Outline each Plasmodium vivax-infected red blood cell.
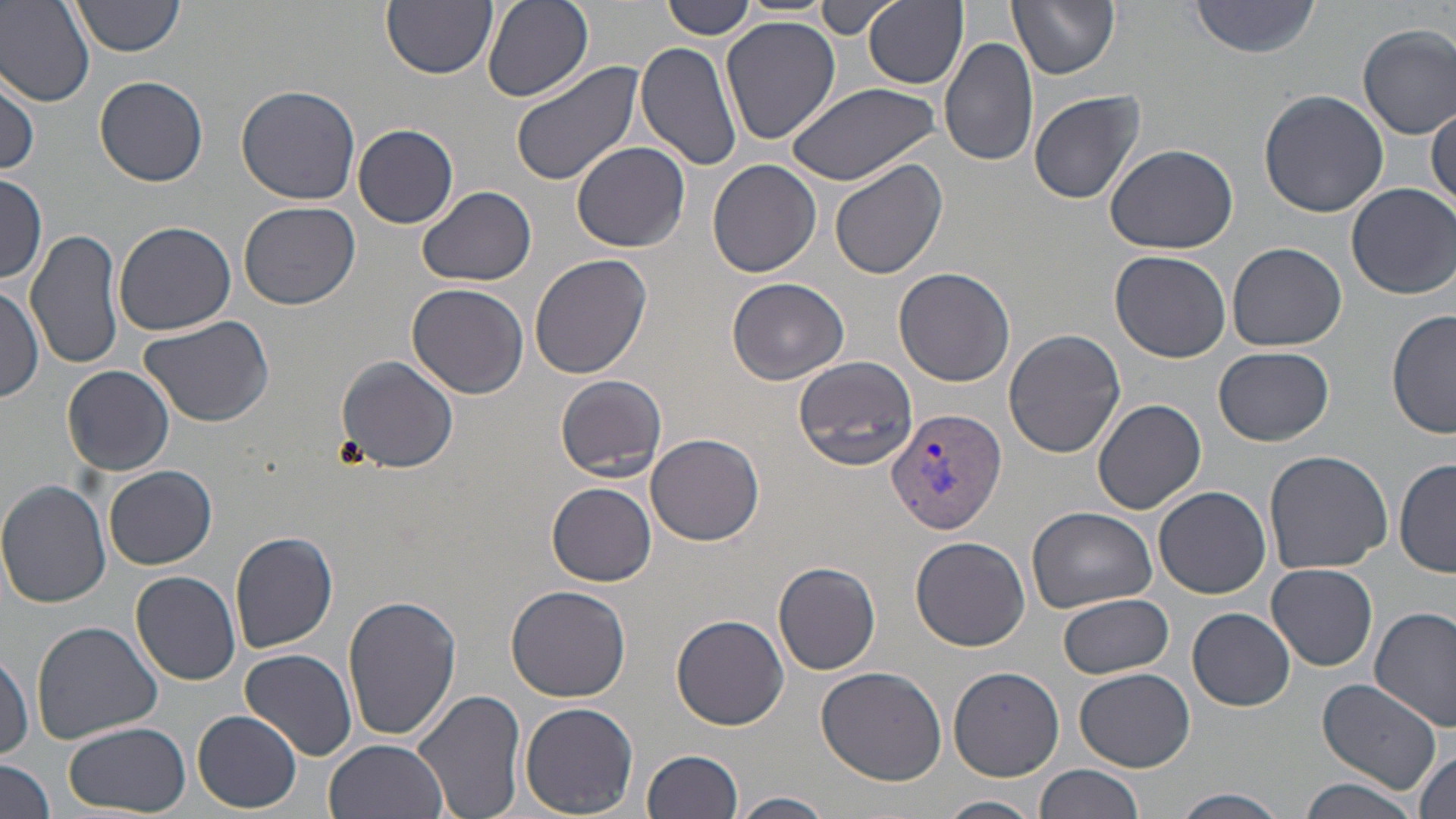

Approximate bounding boxes as (x1,y1)-(x2,y2) corner pairs in pixels.
Plasmodium vivax-infected red blood cells: (884,407)-(1006,538).

Uninfected red blood cell locations: (71,0)-(184,57), (382,0)-(496,77), (865,0)-(968,90), (1008,0)-(1121,80), (1191,0)-(1320,58), (0,1)-(96,107), (482,1)-(593,103), (661,1)-(755,40), (816,2)-(895,40), (720,15)-(841,145), (1358,24)-(1456,139), (939,37)-(1039,171), (635,38)-(741,172), (508,61)-(643,189), (1,73)-(41,179), (94,75)-(209,186), (786,81)-(944,185), (235,84)-(362,206), (1257,89)-(1389,217), (1028,90)-(1145,204), (1427,102)-(1455,217), (353,124)-(459,229), (570,142)-(689,252), (1105,143)-(1239,255), (828,157)-(947,282), (707,158)-(821,278), (0,175)-(47,285), (1347,182)-(1454,299), (416,185)-(538,286), (238,200)-(359,309), (114,218)-(239,336), (26,227)-(125,372), (1226,242)-(1348,352), (1109,250)-(1233,364), (529,252)-(652,379), (892,266)-(1016,387), (726,277)-(850,384), (406,282)-(529,400), (0,285)-(44,404), (1387,309)-(1455,440), (136,313)-(276,427), (1003,329)-(1127,459), (1214,345)-(1334,447), (335,353)-(459,474), (792,356)-(921,472), (63,366)-(176,476), (555,373)-(667,482), (1093,399)-(1208,514), (646,431)-(764,547), (1262,449)-(1392,575), (1395,457)-(1456,577), (103,466)-(218,570), (0,481)-(115,608), (548,482)-(656,586), (1154,485)-(1271,598), (1024,506)-(1159,615), (230,529)-(339,653), (911,536)-(1031,651), (773,560)-(882,676), (1267,561)-(1379,671), (131,570)-(241,685), (506,584)-(631,702), (1059,593)-(1175,678), (342,594)-(461,741), (1370,606)-(1456,734), (1186,607)-(1297,711), (671,614)-(789,731), (32,622)-(165,746), (240,647)-(358,761), (0,651)-(33,760), (814,665)-(947,785), (947,665)-(1066,782), (1074,667)-(1198,772), (1316,679)-(1442,792), (413,687)-(527,819), (519,702)-(640,817), (195,710)-(300,812), (61,721)-(189,815), (325,738)-(449,819), (640,749)-(743,819), (1413,749)-(1453,819), (0,758)-(57,818), (1035,763)-(1144,819), (1296,777)-(1422,819), (1170,790)-(1291,819), (732,792)-(835,819), (936,795)-(1044,819). Slide-level diagnosis: Plasmodium vivax. May-Grünwald-Giemsa-stained preparation. Thin blood film. One field of a larger specimen. Image is 1456×819 pixels. Captured at 1000x magnification. Optical microscopy.